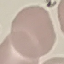
result = no malaria parasites seen
stain = Giemsa
preparation = thin blood film
image type = automatically extracted cell patch, resized to 64 × 64 pixels
capture = smartphone camera at the microscope eyepiece